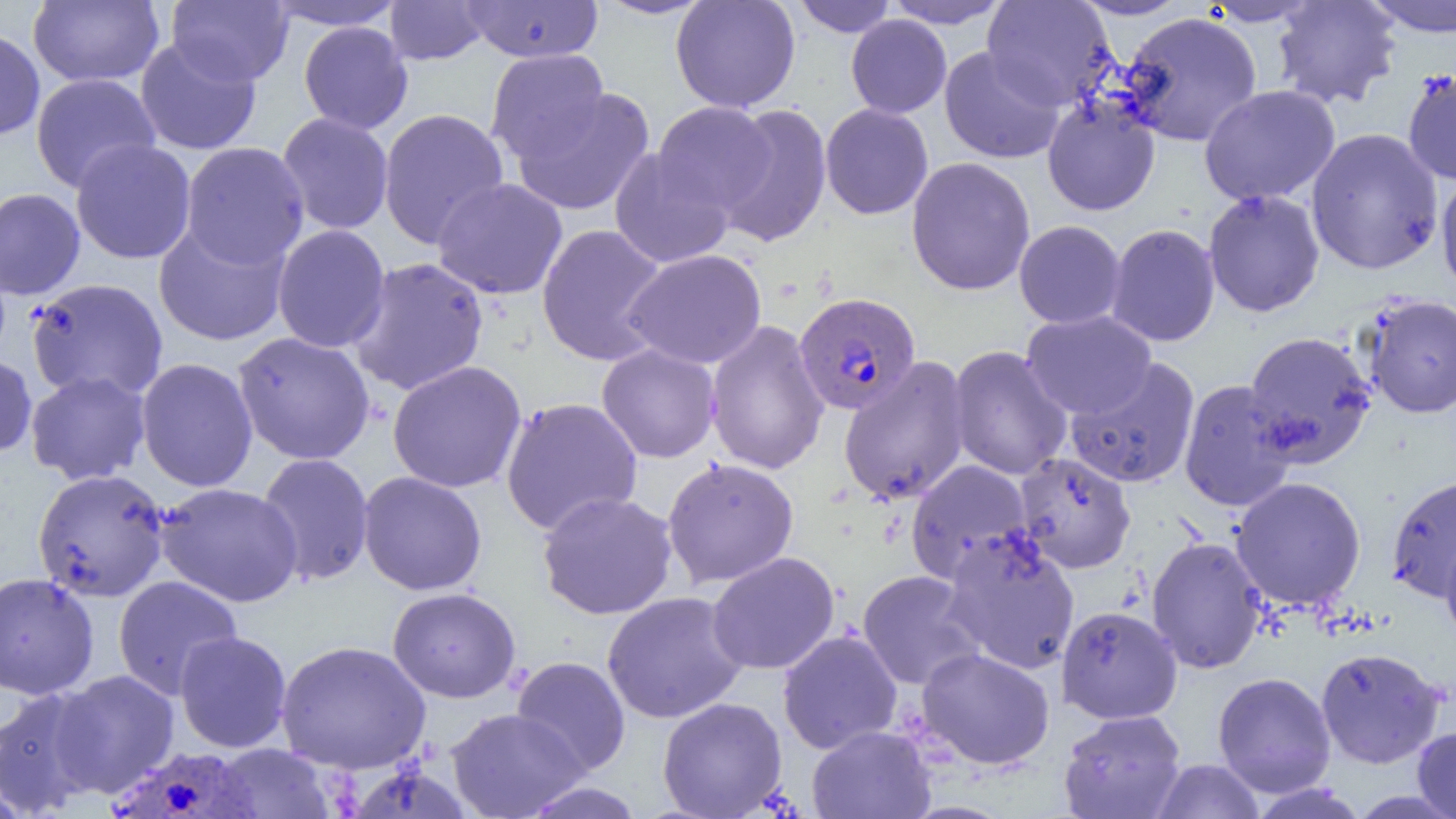

slide-level diagnosis = Plasmodium vivax
image size = 1456×819 pixels
Plasmodium vivax-infected red blood cell locations = approximate bounding boxes as (x1,y1)-(x2,y2) corner pairs in pixels: (794,292)-(921,415), (111,742)-(264,819)
magnification = 1000x
uninfected red blood cell locations = approximate bounding boxes as (x1,y1)-(x2,y2) corner pairs in pixels: (28,0)-(165,87), (166,0)-(294,86), (264,0)-(407,31), (461,0)-(603,63), (592,0)-(714,20), (671,0)-(800,113), (791,0)-(898,37), (883,0)-(1012,29), (1071,0)-(1193,20), (1200,0)-(1323,26), (1272,0)-(1402,110), (1361,0)-(1456,37), (384,1)-(492,65), (982,1)-(1117,109), (1120,12)-(1263,147), (846,15)-(951,118), (298,21)-(413,135), (0,27)-(45,141), (135,36)-(262,155), (939,46)-(1066,164), (485,49)-(610,164), (1403,69)-(1456,185), (30,73)-(160,193), (1199,85)-(1340,206), (508,86)-(656,217), (1042,96)-(1160,216), (653,101)-(776,215), (820,103)-(934,220), (714,104)-(833,247), (378,108)-(510,249), (277,112)-(394,235), (1305,128)-(1444,275), (71,139)-(197,265), (180,142)-(310,269), (609,147)-(735,269), (906,156)-(1036,296), (1436,168)-(1456,301), (432,177)-(568,300), (0,187)-(85,300), (1203,189)-(1325,317), (153,220)-(291,346), (1014,221)-(1126,329), (535,223)-(670,366), (1105,223)-(1221,347), (272,224)-(391,353), (622,249)-(767,369), (347,257)-(489,396), (26,278)-(169,403), (1361,294)-(1456,418), (1021,310)-(1157,419), (705,319)-(830,475), (1243,331)-(1377,469), (232,332)-(376,465), (596,344)-(721,463), (948,345)-(1073,481), (0,353)-(37,459), (837,356)-(972,506), (135,357)-(258,492), (1065,358)-(1201,488), (387,360)-(527,493), (25,370)-(151,485), (1177,379)-(1300,513), (500,397)-(643,535), (1014,452)-(1137,574), (256,453)-(375,587), (661,457)-(800,588), (905,459)-(1034,586), (32,469)-(171,602), (358,471)-(488,596), (1386,475)-(1456,603), (1229,476)-(1367,611), (155,482)-(304,607), (537,491)-(678,620), (940,530)-(1081,675), (1440,535)-(1456,649), (1146,536)-(1268,674), (706,551)-(840,675), (856,570)-(986,691), (0,572)-(99,700), (112,575)-(243,700), (387,587)-(521,703), (602,591)-(749,724), (1056,605)-(1182,724), (777,630)-(903,754), (175,631)-(292,753), (275,640)-(431,773), (915,647)-(1056,770), (1315,647)-(1446,769), (511,656)-(631,777), (51,669)-(180,797), (1212,672)-(1337,797), (0,685)-(105,817), (657,696)-(787,818), (445,707)-(587,818), (1058,709)-(1187,819), (806,725)-(936,819), (1412,725)-(1456,819), (209,743)-(336,818), (1150,759)-(1266,818), (519,782)-(647,819)
field of view = single
modality = light microscopy
preparation = thin blood smear